Give the position of every malaria parasite.
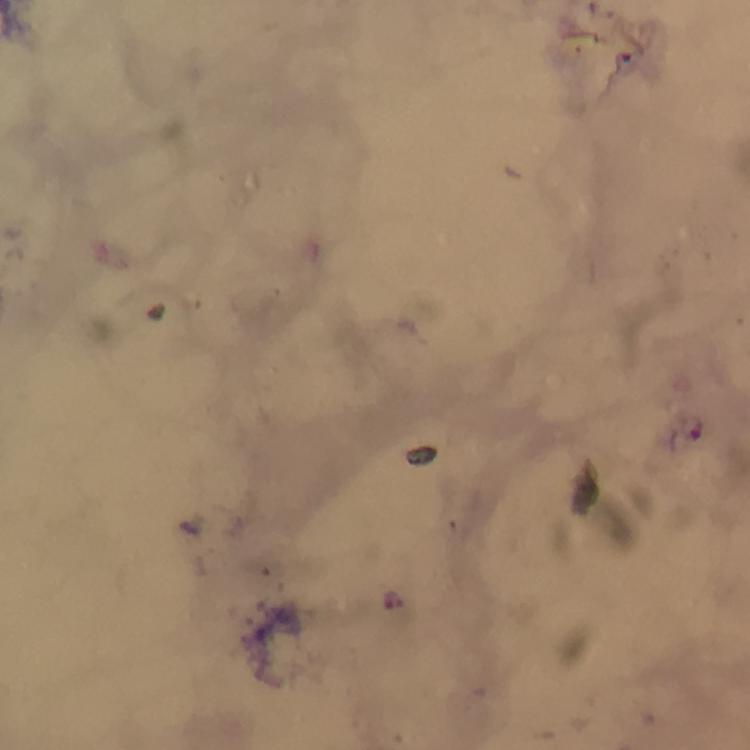

Approximate centers as {x, y} in pixels.
Malaria parasites: {394, 601}.

Photographed with a smartphone mounted on the microscope. At 100x magnification. From a diagnostic examination for malaria. A crop from one field of view. Giemsa stain. Image is 750×750 pixels. Thick blood smear. Immersion oil was used.